Report the malaria status of this cell.
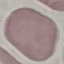
It is uninfected.

Cell patch, automatically extracted from a larger field of view and resized to 64 × 64 pixels. Thin blood film. Acquired by smartphone through the microscope eyepiece. Giemsa stain.